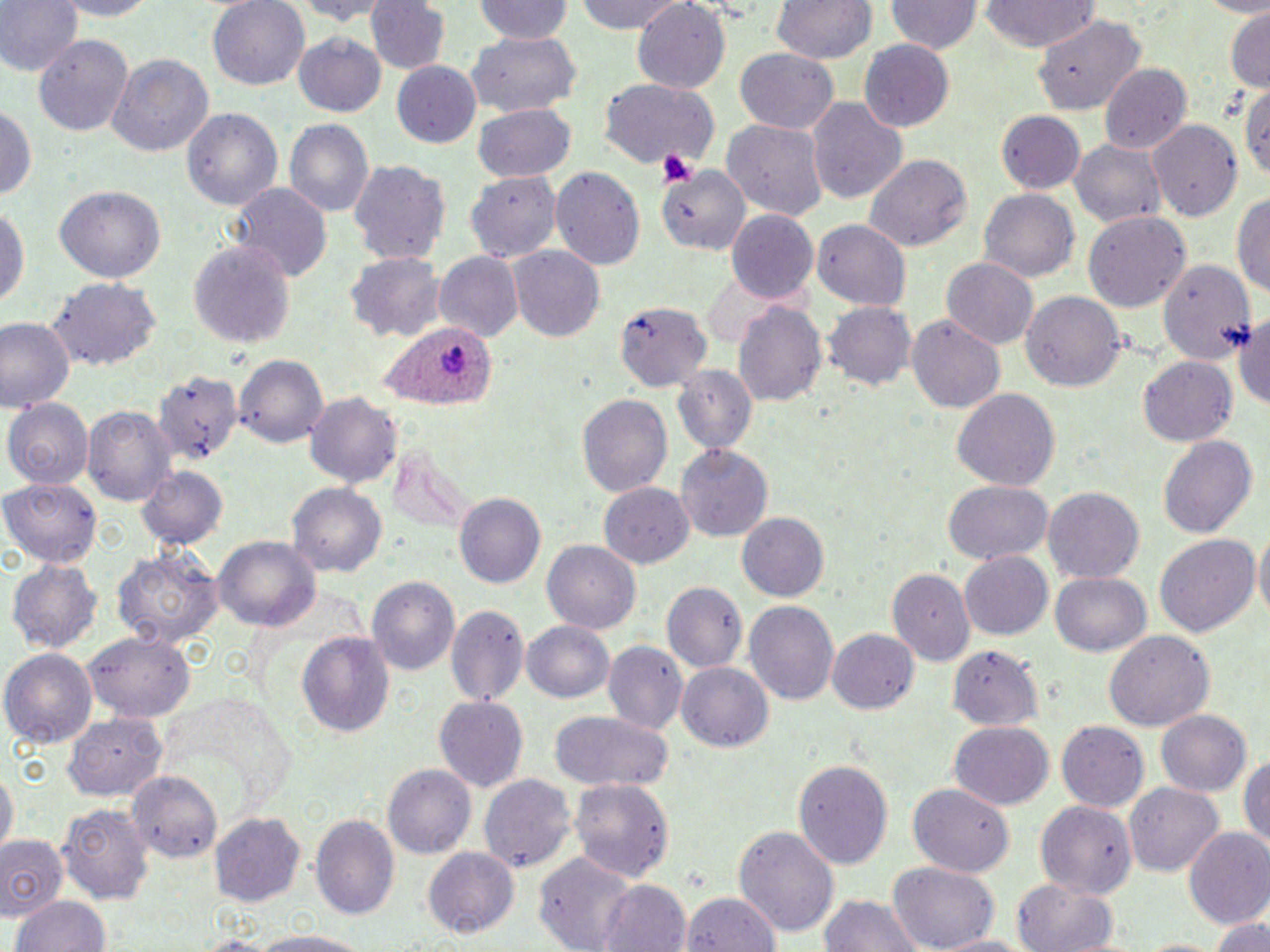
Summary:
  - Coordinate format: approximate bounding boxes as [x1, y1, x2, y2] in pixels
  - Platelet locations: [657, 145, 699, 189]
  - Plasmodium ovale-infected red blood cell locations: [383, 320, 494, 408]
  - Uninfected red blood cell locations: [0, 0, 80, 77], [50, 0, 158, 19], [208, 0, 309, 91], [283, 0, 392, 23], [365, 0, 449, 75], [472, 0, 577, 43], [575, 0, 688, 33], [770, 0, 877, 63], [886, 0, 980, 55], [981, 0, 1099, 53], [628, 3, 732, 93], [1224, 9, 1270, 93], [1035, 15, 1147, 113], [465, 31, 582, 111], [32, 33, 131, 136], [293, 33, 387, 117], [860, 38, 955, 131], [733, 49, 840, 135], [105, 50, 214, 156], [392, 64, 482, 147], [1098, 65, 1190, 154], [1238, 78, 1270, 180], [600, 81, 717, 170], [805, 98, 907, 205], [0, 101, 36, 208], [472, 106, 577, 181], [183, 108, 283, 211], [995, 111, 1086, 194], [284, 120, 372, 222], [721, 120, 829, 220], [1151, 120, 1243, 219], [1070, 137, 1164, 229], [865, 156, 972, 255], [351, 160, 448, 264], [658, 164, 749, 256], [551, 167, 644, 272], [465, 170, 560, 261], [232, 184, 331, 284], [55, 186, 165, 284], [1234, 188, 1270, 301], [977, 189, 1079, 285], [0, 202, 30, 315], [725, 210, 818, 305], [1084, 211, 1191, 312], [813, 221, 911, 311], [188, 242, 295, 346], [510, 246, 606, 342], [435, 251, 523, 344], [345, 253, 444, 344], [1158, 255, 1256, 366], [942, 258, 1037, 348], [701, 274, 792, 351], [46, 278, 162, 371], [1020, 293, 1125, 391], [614, 299, 710, 393], [735, 299, 826, 406], [824, 301, 915, 392], [1233, 307, 1270, 416], [907, 315, 1006, 414], [0, 317, 75, 413], [234, 354, 328, 449], [1138, 354, 1237, 446], [672, 365, 758, 456], [152, 368, 243, 471], [953, 389, 1058, 494], [577, 392, 672, 496], [305, 393, 400, 490], [7, 399, 92, 487], [85, 404, 176, 508], [1158, 434, 1259, 540], [675, 442, 772, 538], [385, 446, 475, 531], [137, 464, 227, 550], [2, 480, 102, 567], [943, 481, 1051, 565], [598, 482, 691, 569], [290, 484, 385, 579], [1044, 487, 1144, 581], [454, 491, 546, 588], [738, 510, 831, 601], [1252, 526, 1270, 629], [1153, 534, 1259, 639], [213, 537, 319, 632], [544, 539, 641, 633], [115, 545, 221, 649], [959, 551, 1053, 640], [8, 560, 101, 653], [887, 567, 972, 661], [1051, 571, 1150, 657], [368, 574, 464, 677], [661, 581, 746, 673], [744, 602, 838, 705], [444, 604, 527, 707], [520, 619, 616, 703], [295, 628, 396, 737], [829, 629, 917, 715], [85, 632, 192, 724], [1105, 632, 1214, 731], [601, 640, 688, 734], [948, 645, 1043, 730], [2, 648, 98, 746], [677, 662, 774, 752], [157, 691, 301, 815], [434, 696, 530, 792], [1154, 708, 1253, 797], [549, 710, 676, 792], [63, 713, 167, 801], [1057, 720, 1150, 812], [948, 723, 1054, 809], [1239, 748, 1270, 852], [795, 758, 893, 870], [0, 764, 16, 855], [384, 765, 475, 857], [128, 770, 225, 864], [480, 774, 576, 875], [570, 779, 675, 883], [1129, 782, 1220, 878], [909, 783, 1014, 875], [1035, 800, 1134, 896], [59, 803, 153, 906], [209, 812, 307, 905], [312, 812, 401, 923], [736, 826, 838, 939], [1184, 828, 1270, 930], [0, 835, 68, 920], [423, 846, 520, 940], [532, 853, 637, 947], [891, 861, 998, 950], [1014, 877, 1121, 952], [599, 878, 691, 952], [816, 891, 925, 952], [686, 892, 781, 952], [11, 894, 110, 952], [1212, 910, 1269, 952], [247, 929, 377, 952], [930, 931, 1031, 952], [1136, 935, 1220, 952]
  - Slide-level diagnosis: Plasmodium ovale
  - Field of view: one of a larger specimen
  - Preparation: thin blood smear
  - Magnification: 1000x
  - Image size: 1270×952 pixels
  - Stain: May-Grünwald-Giemsa
  - Modality: optical microscopy